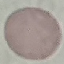
{
  "malaria_status": "uninfected",
  "capture": "smartphone through the microscope eyepiece",
  "image_type": "cell patch, automatically extracted from a larger field of view and resized to 64 × 64 pixels",
  "stain": "Giemsa",
  "preparation": "thin blood smear"
}